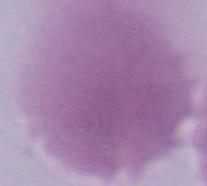
modality = micrograph
identification = erythrocyte
magnification = 1000x